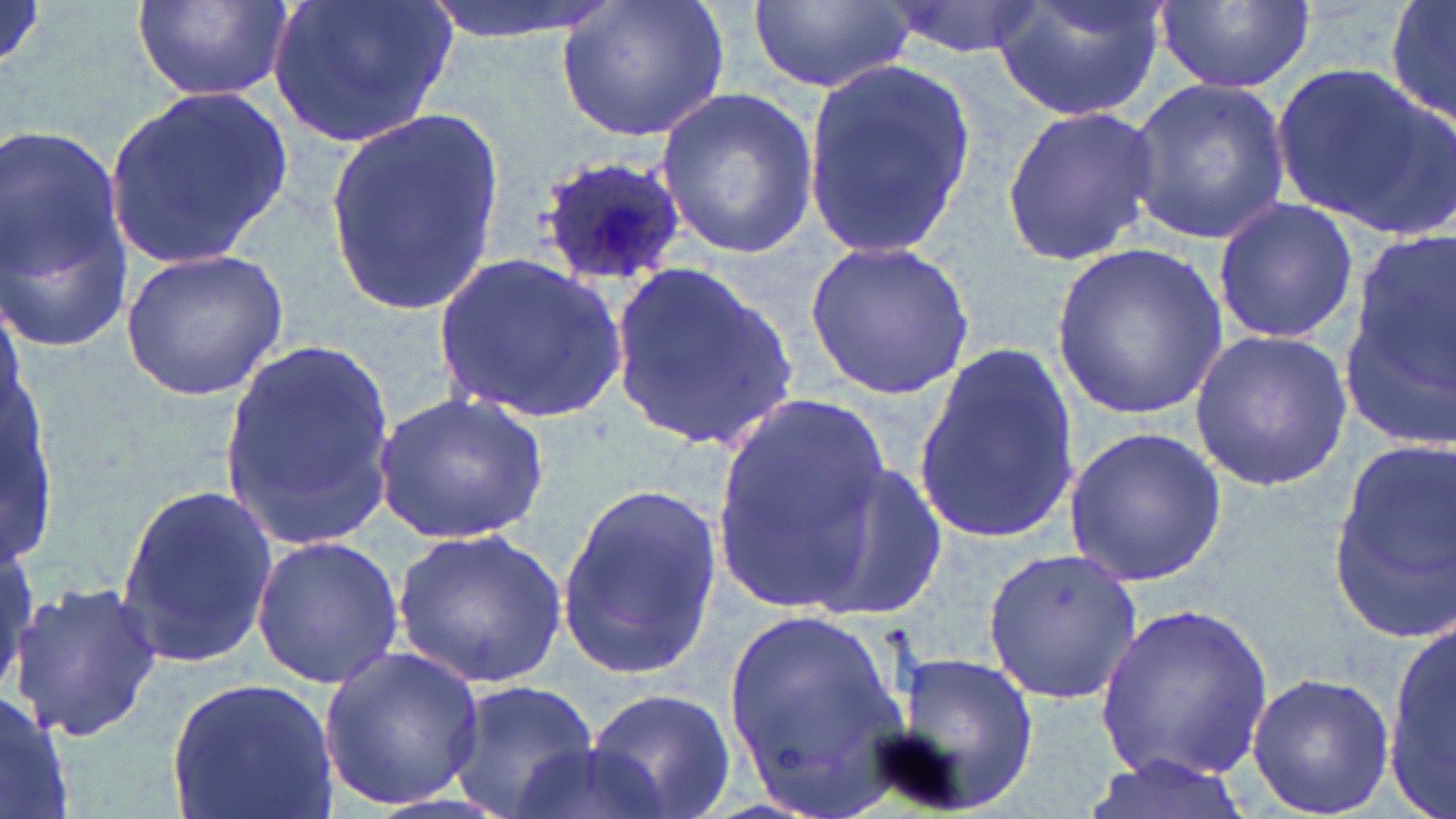

slide_level_diagnosis: Plasmodium ovale
image_size: 1456×819 pixels
magnification: 1000x
uninfected_red_blood_cell_locations: 'approximate bounding boxes as (x1,y1)-(x2,y2) corner pairs in pixels: (133,0)-(291,102), (263,0)-(458,149), (418,0)-(617,43), (552,0)-(734,146), (746,0)-(914,96), (883,0)-(1046,59), (991,0)-(1171,123), (1385,0)-(1456,131), (1157,2)-(1312,92), (801,59)-(973,261), (1272,59)-(1455,241), (1127,74)-(1292,245), (106,86)-(296,271), (655,90)-(818,257), (1001,104)-(1162,267), (325,110)-(506,315), (1,121)-(135,351), (1211,200)-(1359,345), (804,238)-(978,401), (1053,242)-(1227,415), (1338,242)-(1455,448), (119,247)-(291,402), (431,253)-(630,426), (608,261)-(804,452), (1188,327)-(1354,490), (219,338)-(398,542), (912,343)-(1078,537), (372,391)-(551,545), (708,396)-(891,608), (1062,427)-(1226,586), (1326,434)-(1456,639), (802,461)-(952,618), (113,482)-(277,666), (555,484)-(722,676), (390,528)-(567,687), (250,533)-(406,690), (977,542)-(1147,703), (8,581)-(164,741), (1096,604)-(1277,782), (719,607)-(915,813), (1387,607)-(1454,819), (318,644)-(486,811), (883,651)-(1041,817), (1244,672)-(1395,815), (164,675)-(336,819), (445,679)-(602,819), (0,683)-(77,819), (585,687)-(735,819), (512,739)-(672,819), (1076,755)-(1256,819)'
preparation: thin blood film
field_of_view: one of a larger specimen
modality: light microscopy
plasmodium_ovale_infected_red_blood_cell_locations: 'approximate bounding boxes as (x1,y1)-(x2,y2) corner pairs in pixels: (535,153)-(693,291)'
stain: May-Grünwald-Giemsa